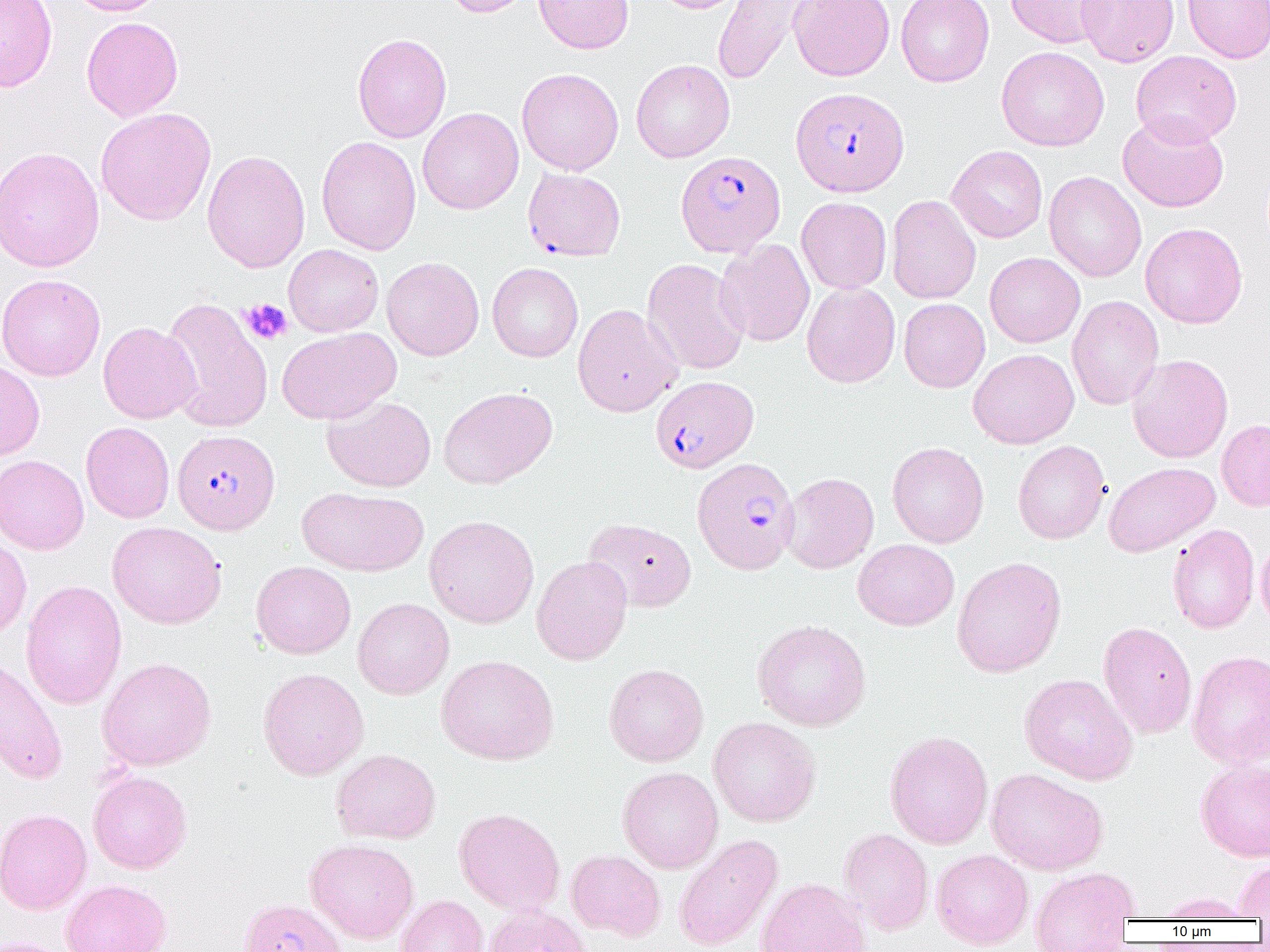

Approximate bounding boxes as (x1,y1)-(x2,y2) corner pairs in pixels. Plasmodium falciparum-infected red blood cell locations: (790,87)-(909,196), (675,151)-(785,257), (523,168)-(626,261), (651,376)-(758,473), (172,429)-(280,534), (692,457)-(799,574). Platelet locations: (241,298)-(293,344). Uninfected red blood cell locations: (0,0)-(57,92), (67,0)-(168,16), (443,0)-(537,17), (534,0)-(634,54), (652,0)-(748,14), (712,0)-(813,86), (788,0)-(894,81), (896,0)-(995,87), (1005,0)-(1112,48), (1076,0)-(1179,67), (1183,0)-(1270,63), (82,16)-(183,121), (352,33)-(452,143), (996,46)-(1109,151), (1130,50)-(1242,147), (631,59)-(735,162), (517,68)-(624,176), (418,107)-(523,214), (95,108)-(216,226), (1117,112)-(1229,212), (316,136)-(421,255), (946,145)-(1047,243), (0,146)-(105,272), (202,149)-(310,273), (1043,171)-(1146,282), (886,195)-(981,304), (796,197)-(891,293), (1140,222)-(1248,328), (715,239)-(815,347), (283,244)-(383,337), (985,252)-(1085,347), (382,256)-(484,361), (642,258)-(749,376), (487,262)-(583,362), (0,273)-(106,381), (801,282)-(900,388), (1067,295)-(1164,411), (161,298)-(273,433), (899,298)-(990,392), (573,303)-(682,417), (98,321)-(201,424), (277,327)-(401,425), (968,348)-(1079,449), (1127,354)-(1233,463), (0,360)-(45,460), (438,387)-(558,489), (322,395)-(436,492), (1217,419)-(1270,511), (81,421)-(175,523), (1012,440)-(1110,544), (887,442)-(989,548), (0,454)-(89,555), (1104,462)-(1219,556), (781,472)-(879,574), (298,487)-(427,577), (425,515)-(539,628), (584,518)-(696,612), (107,521)-(226,629), (1167,524)-(1260,633), (0,534)-(32,638), (1255,536)-(1270,636), (853,539)-(959,630), (531,555)-(632,665), (952,556)-(1066,677), (251,561)-(356,658), (20,579)-(127,710), (353,598)-(454,700), (752,619)-(871,731), (1098,622)-(1197,738), (1187,650)-(1270,768), (0,654)-(68,785), (436,654)-(558,765), (97,657)-(216,770), (603,663)-(709,766), (258,667)-(369,780), (1019,673)-(1138,784), (708,716)-(821,827), (884,730)-(993,849), (331,748)-(441,844), (1196,759)-(1270,862), (617,766)-(723,873), (986,767)-(1108,875), (88,769)-(192,873), (454,807)-(565,914), (0,808)-(91,915), (838,828)-(934,934), (674,834)-(782,951), (305,838)-(419,943), (566,849)-(666,941), (931,849)-(1033,950), (1233,859)-(1270,920), (1029,867)-(1140,950), (756,878)-(870,952), (60,879)-(171,952), (1155,892)-(1254,921), (396,895)-(489,952), (238,898)-(348,952), (484,904)-(594,952), (0,937)-(74,952). Slide-level diagnosis: Plasmodium falciparum. Single field of view. Thin blood smear. 1000x magnification. Image is 1270×952 pixels. Optical microscopy.